Look for parasitized red blood cells.
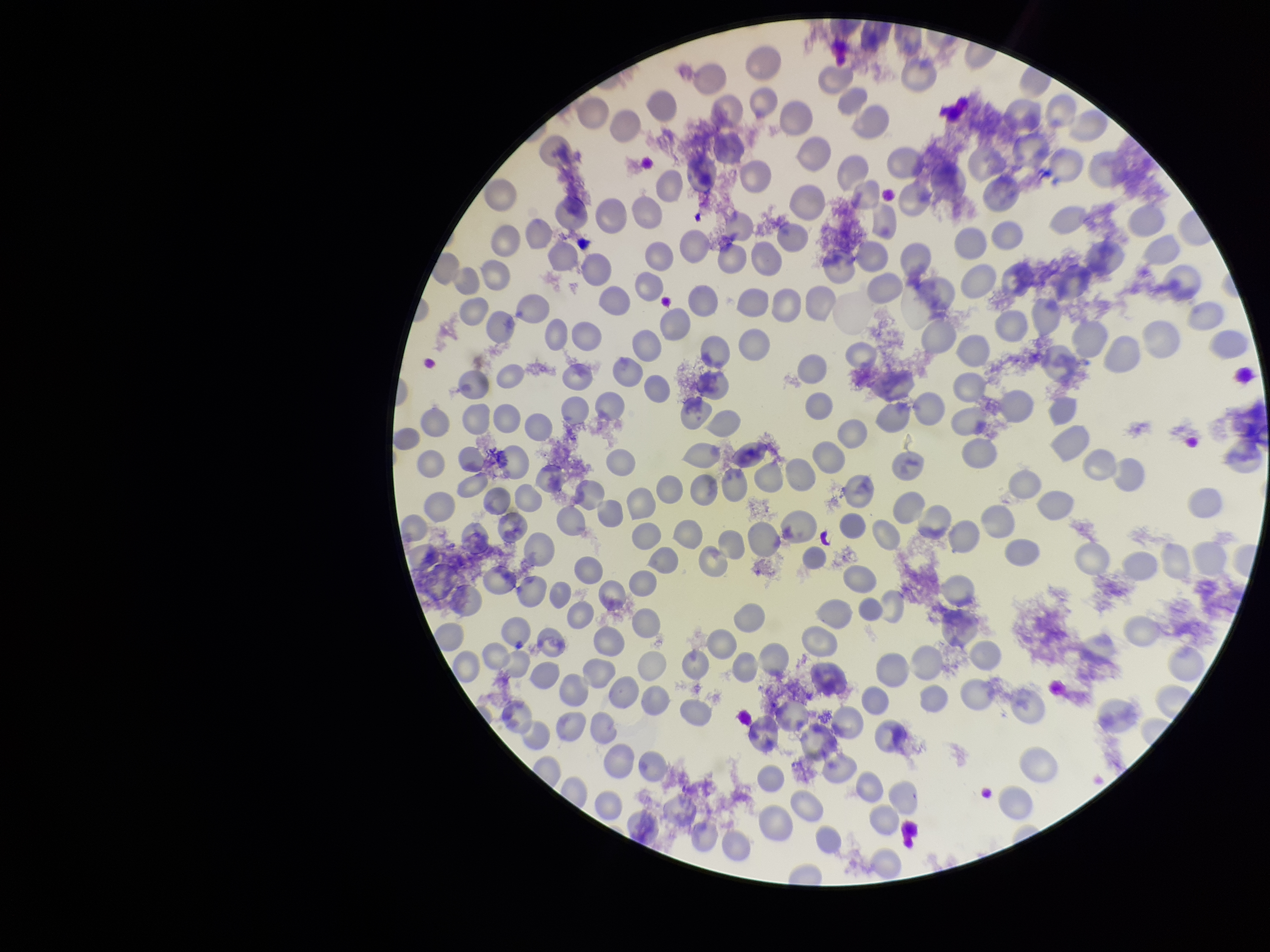
None detected.

One field from this slide. Patient malaria status: positive. Red blood cell count: 267. Stained with Giemsa. Image is 1270×952 pixels. Preparation: thin smear. Parasitized red blood cell count: 0. Species reported for this patient: Plasmodium falciparum. Smartphone photograph taken through the eyepiece of a microscope.